Locate malaria parasites and leukocytes.
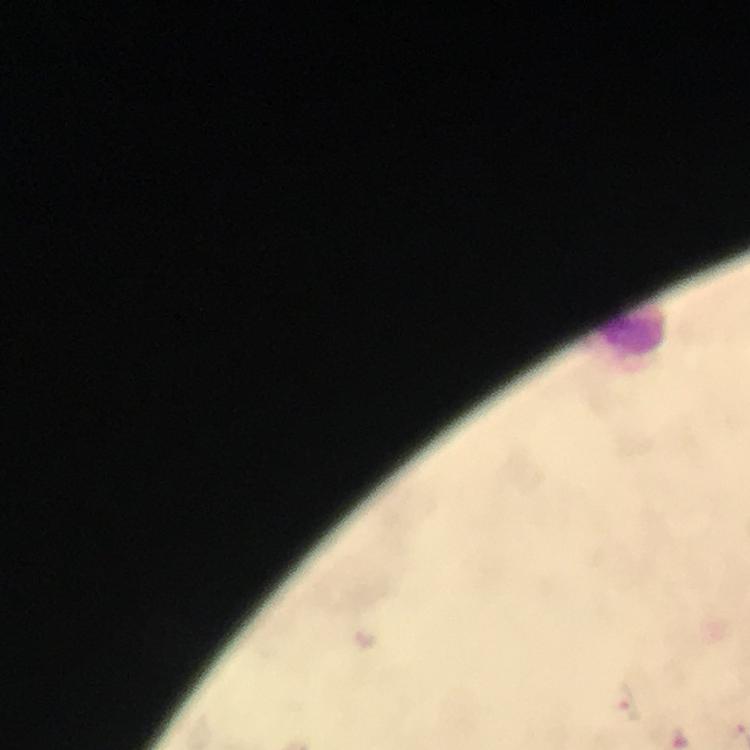

Approximate object centers, in pixels from the top-left corner.
Malaria parasites: (x=365, y=640), (x=629, y=702).
Leukocytes: (x=632, y=334).

cropped_from: one field of view
immersion_oil: used
stain: Giemsa
magnification: 100x
preparation: thick blood film
capture: smartphone photograph through a microscope
image_size: 750×750 pixels
context: from a diagnostic examination for malaria